Assess this cell for malaria.
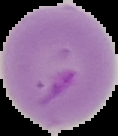
It is parasitized.

From a thin blood smear. Image is 118×136 pixels. The area outside the segmented cell region is set to black.